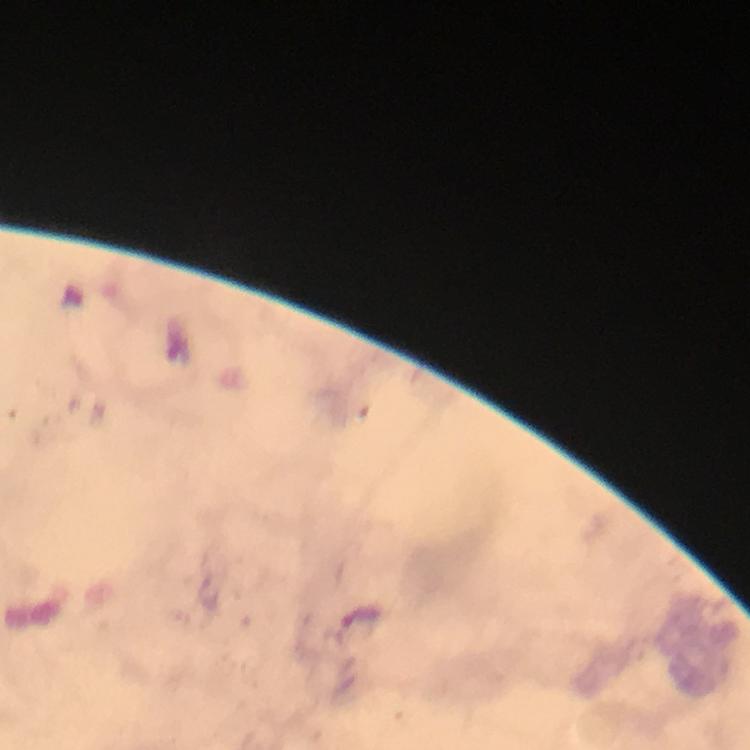

preparation: thick smear
plasmodium_parasite_locations: 'approximate centers as (x, y) in pixels: (359, 616)'
stain: Giemsa
magnification: 100x
cropped_from: one field of view
image_size: 750×750 pixels
capture: smartphone photograph through a microscope
context: from a malaria diagnostic workup
immersion_oil: applied